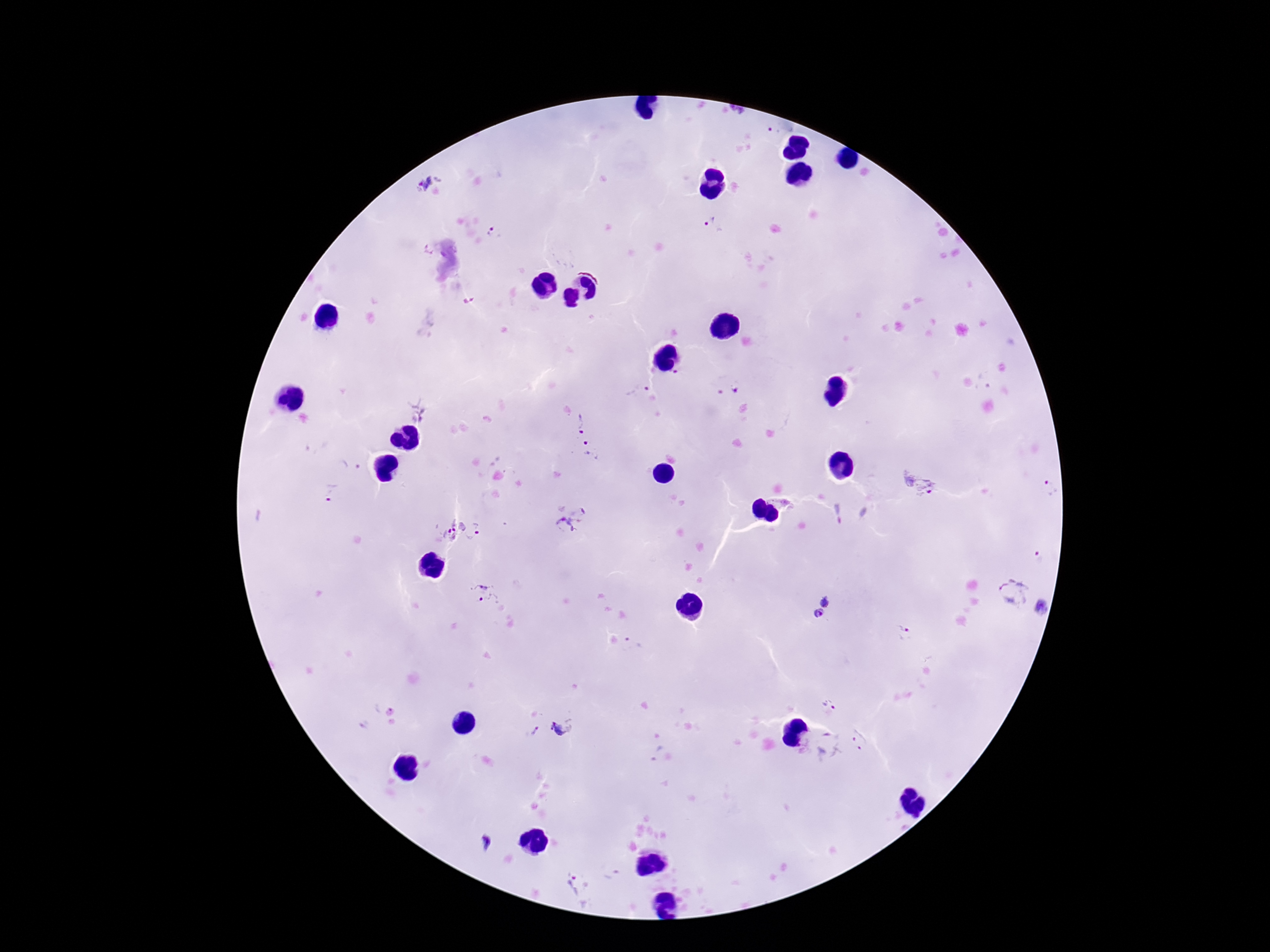
Approximate centers as (x, y) in pixels.
Summary:
  - Plasmodium parasite locations: (430, 183), (712, 224), (494, 233), (735, 387), (419, 409), (579, 422), (593, 451), (351, 467), (919, 484), (1050, 489), (331, 492), (569, 518), (451, 530), (480, 533), (1038, 559), (1013, 591), (488, 593), (827, 600), (1043, 608), (819, 614), (905, 632), (829, 708), (564, 726), (535, 731), (862, 737), (831, 747), (482, 842), (579, 890)
  - Patient malaria status: positive
  - Preparation: thick peripheral-blood smear
  - Image size: 1270×952 pixels
  - Magnification: 100x
  - Capture: smartphone camera through the microscope eyepiece
  - Field of view: one from this slide
  - Stain: Giemsa